Point out every Plasmodium parasite and every leukocyte.
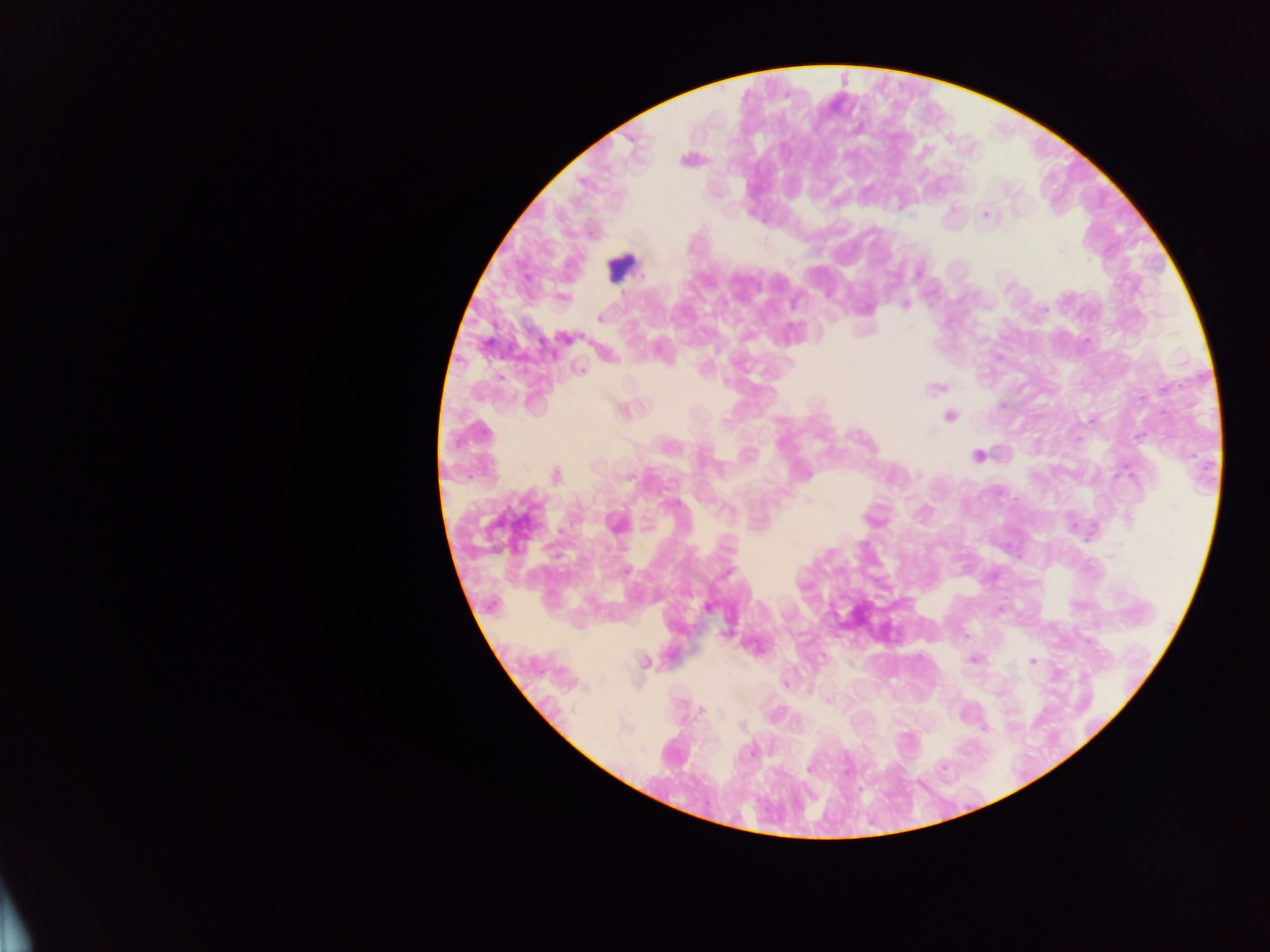
Approximate centers as (x, y) in pixels.
Plasmodium parasites: (689, 159), (987, 214), (561, 297), (904, 304), (600, 318), (566, 337), (577, 370), (935, 388), (625, 409), (949, 415), (977, 455), (554, 475), (808, 502), (616, 524), (708, 606), (974, 658), (643, 661), (1032, 661), (785, 682), (828, 700), (702, 710).
Leukocytes: (620, 267).

Sample from Ghana. Single field of view. Image is 1270×952 pixels. Mobile-phone photograph taken through the microscope. Thick blood film.